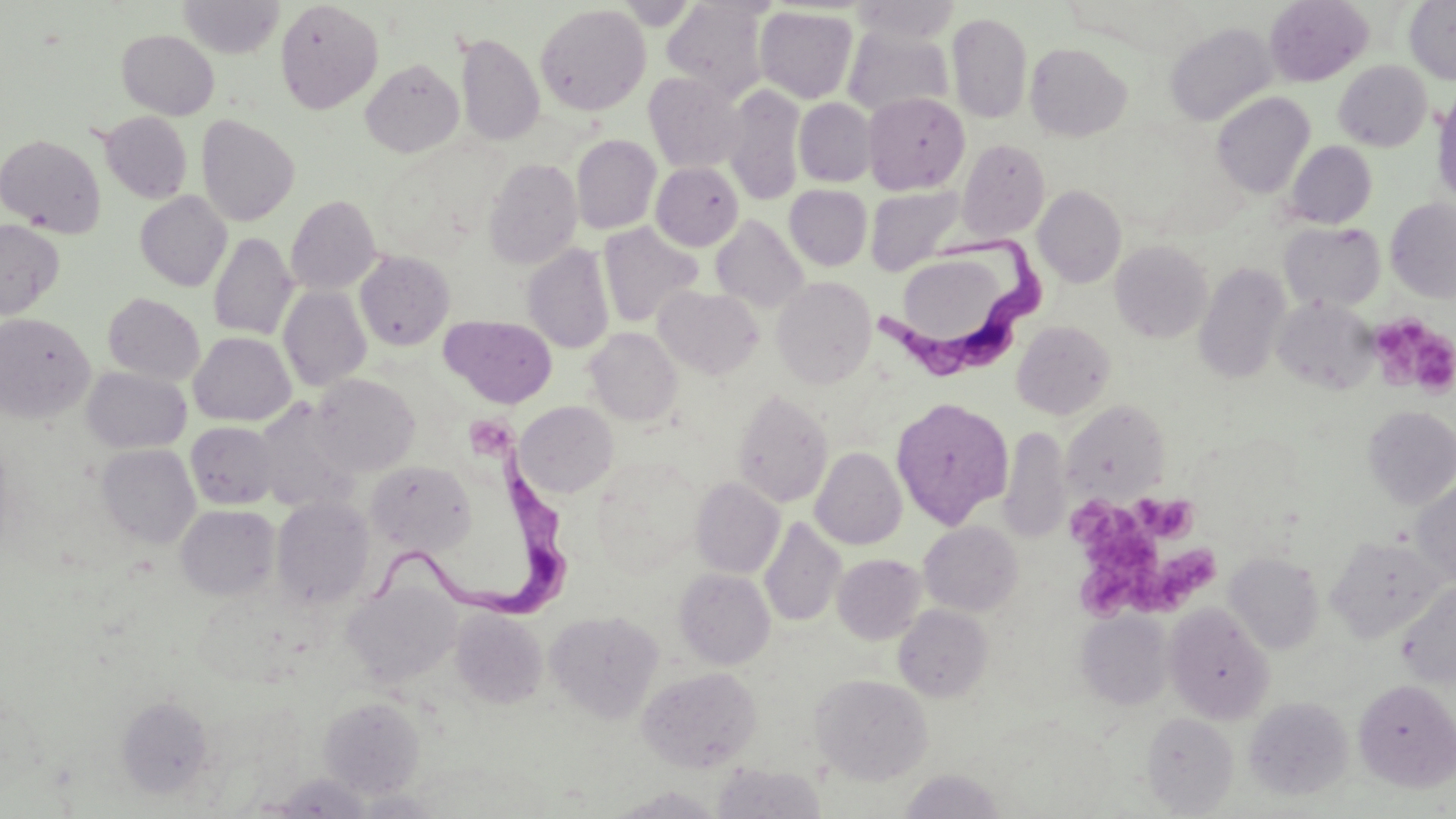
{
  "slide_level_diagnosis": "Trypanosoma brucei",
  "platelet_locations": "approximate bounding boxes as (x1,y1)-(x2,y2) corner pairs in pixels: (1369,315)-(1455,397), (464,412)-(519,463), (1130,493)-(1197,542), (1068,499)-(1142,550), (1150,547)-(1215,611), (1079,561)-(1146,621)",
  "magnification": "1000x",
  "modality": "light microscopy",
  "field_of_view": "single",
  "trypanosoma_brucei_locations": "approximate bounding boxes as (x1,y1)-(x2,y2) corner pairs in pixels: (874,233)-(1056,391), (367,454)-(568,625)",
  "uninfected_red_blood_cell_locations": "approximate bounding boxes as (x1,y1)-(x2,y2) corner pairs in pixels: (178,0)-(284,58), (275,0)-(383,113), (613,0)-(701,29), (1264,0)-(1373,86), (1404,0)-(1456,84), (662,1)-(770,99), (849,1)-(962,43), (535,5)-(651,116), (754,6)-(858,103), (947,11)-(1033,124), (1165,21)-(1278,126), (843,28)-(953,118), (117,29)-(219,119), (456,32)-(544,146), (1024,42)-(1132,141), (361,59)-(464,158), (1334,61)-(1432,151), (643,72)-(747,173), (721,84)-(805,206), (1432,89)-(1456,207), (863,92)-(969,194), (1212,92)-(1315,199), (794,98)-(876,187), (99,111)-(192,204), (196,114)-(300,226), (0,134)-(106,237), (571,134)-(661,234), (957,139)-(1050,241), (1285,141)-(1377,228), (484,157)-(582,269), (651,162)-(743,251), (785,184)-(872,270), (866,185)-(966,275), (1033,185)-(1126,288), (135,191)-(231,291), (286,195)-(381,294), (1385,198)-(1456,302), (711,215)-(808,312), (0,220)-(64,320), (1279,221)-(1385,311), (598,222)-(703,328), (208,232)-(298,340), (1110,240)-(1213,343), (523,243)-(614,354), (355,251)-(455,350), (900,255)-(1007,351), (1194,262)-(1290,385), (772,276)-(876,388), (278,286)-(371,391), (654,286)-(763,378), (103,292)-(205,385), (1271,296)-(1378,395), (0,312)-(95,423), (440,315)-(557,409), (1012,321)-(1116,419), (586,328)-(682,426), (188,331)-(295,425), (83,367)-(191,453), (310,374)-(419,476), (732,388)-(834,508), (890,397)-(1013,529), (253,398)-(359,514), (1061,400)-(1169,501), (515,401)-(618,497), (1362,405)-(1456,508), (186,421)-(278,509), (999,426)-(1071,543), (96,443)-(200,548), (811,447)-(907,550), (589,458)-(704,576), (364,461)-(476,556), (691,477)-(785,578), (1411,477)-(1456,587), (272,496)-(375,610), (176,504)-(280,601), (759,516)-(846,627), (919,521)-(1022,616), (1326,535)-(1447,642), (1224,552)-(1324,654), (833,554)-(926,644), (674,568)-(776,669), (1397,580)-(1456,689), (346,583)-(460,688), (1164,603)-(1274,723), (893,605)-(993,701), (451,609)-(547,708), (545,610)-(664,723), (1077,610)-(1174,709), (636,665)-(762,772), (811,674)-(932,784), (1353,679)-(1456,792), (117,695)-(214,799), (319,696)-(425,798), (1243,696)-(1353,801), (1141,712)-(1239,817), (713,762)-(826,819), (899,769)-(1006,818), (609,786)-(727,818)",
  "stain": "May-Grünwald-Giemsa",
  "image_size": "1456×819 pixels",
  "preparation": "thin blood film"
}